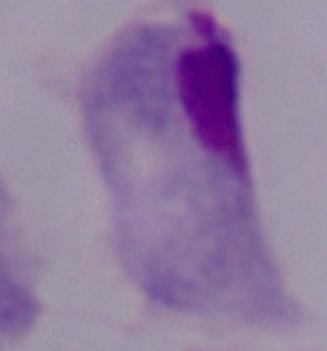

Summary:
  - Identification: trichomonad
  - Modality: micrograph
  - Magnification: 1000x